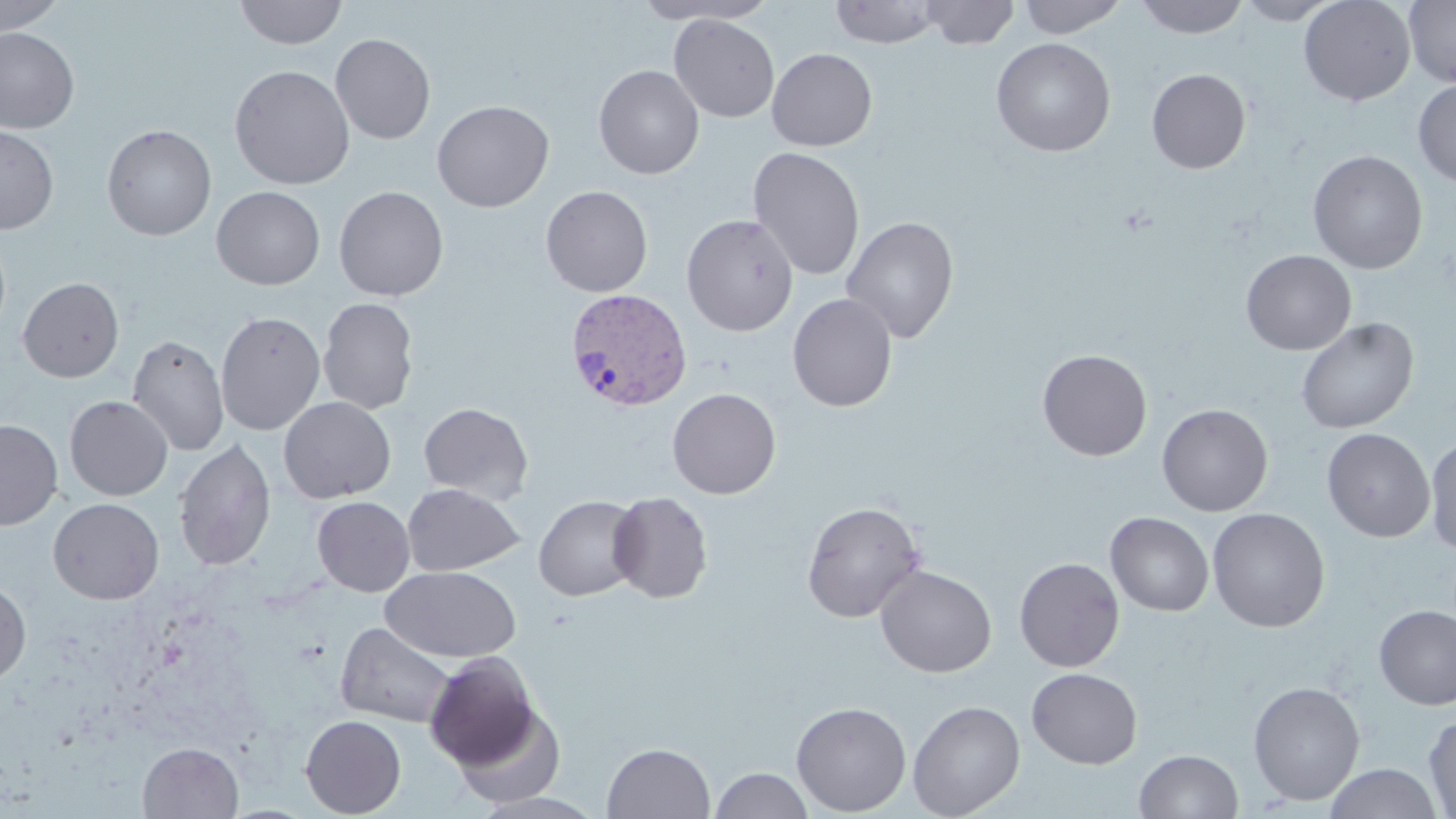
Approximate bounding boxes as (x1, y1, x2, y2) in pixels. Plasmodium vivax-infected red blood cell locations: (564, 288, 694, 412). Uninfected red blood cell locations: (0, 0, 67, 35), (234, 0, 347, 49), (632, 0, 775, 24), (920, 0, 1020, 49), (1017, 0, 1128, 38), (1133, 0, 1251, 39), (1235, 0, 1343, 25), (1298, 0, 1416, 106), (1404, 0, 1456, 88), (829, 1, 945, 47), (669, 14, 779, 122), (0, 27, 80, 134), (331, 33, 436, 144), (991, 37, 1115, 157), (767, 47, 877, 151), (229, 64, 355, 190), (594, 64, 704, 179), (1146, 68, 1251, 174), (1413, 79, 1456, 187), (431, 99, 554, 211), (0, 124, 58, 234), (101, 124, 217, 240), (748, 146, 865, 280), (1308, 150, 1428, 273), (334, 185, 449, 301), (540, 185, 653, 297), (211, 186, 325, 290), (328, 186, 433, 415), (681, 214, 798, 336), (841, 216, 959, 343), (0, 231, 11, 343), (1241, 250, 1356, 355), (17, 277, 124, 382), (787, 293, 898, 412), (318, 297, 419, 415), (216, 311, 325, 435), (1296, 317, 1418, 434), (127, 334, 230, 456), (1037, 349, 1153, 461), (667, 388, 781, 499), (65, 395, 173, 500), (278, 396, 397, 503), (301, 397, 404, 596), (418, 402, 535, 505), (1157, 403, 1273, 516), (0, 419, 62, 529), (1321, 428, 1435, 542), (1425, 435, 1456, 557), (173, 438, 276, 572), (402, 483, 524, 576), (607, 491, 713, 603), (533, 495, 643, 601), (312, 496, 415, 596), (47, 498, 164, 604), (801, 500, 926, 623), (1207, 507, 1330, 632), (1105, 512, 1214, 616), (1014, 557, 1125, 672), (382, 565, 520, 663), (875, 565, 996, 677), (0, 580, 31, 684), (1373, 604, 1456, 710), (335, 621, 456, 728), (424, 652, 540, 769), (1026, 667, 1142, 768), (1248, 681, 1365, 805), (908, 699, 1026, 818), (791, 701, 911, 816), (450, 704, 567, 806), (300, 714, 406, 817), (1423, 714, 1456, 817), (137, 741, 243, 818), (602, 742, 715, 819), (1134, 749, 1243, 818), (1324, 763, 1442, 819), (710, 767, 813, 819). Slide-level diagnosis: Plasmodium vivax. May-Grünwald-Giemsa stain. Thin blood smear. 1000x magnification. Light microscopy. Image is 1456×819 pixels. One field of a larger specimen.